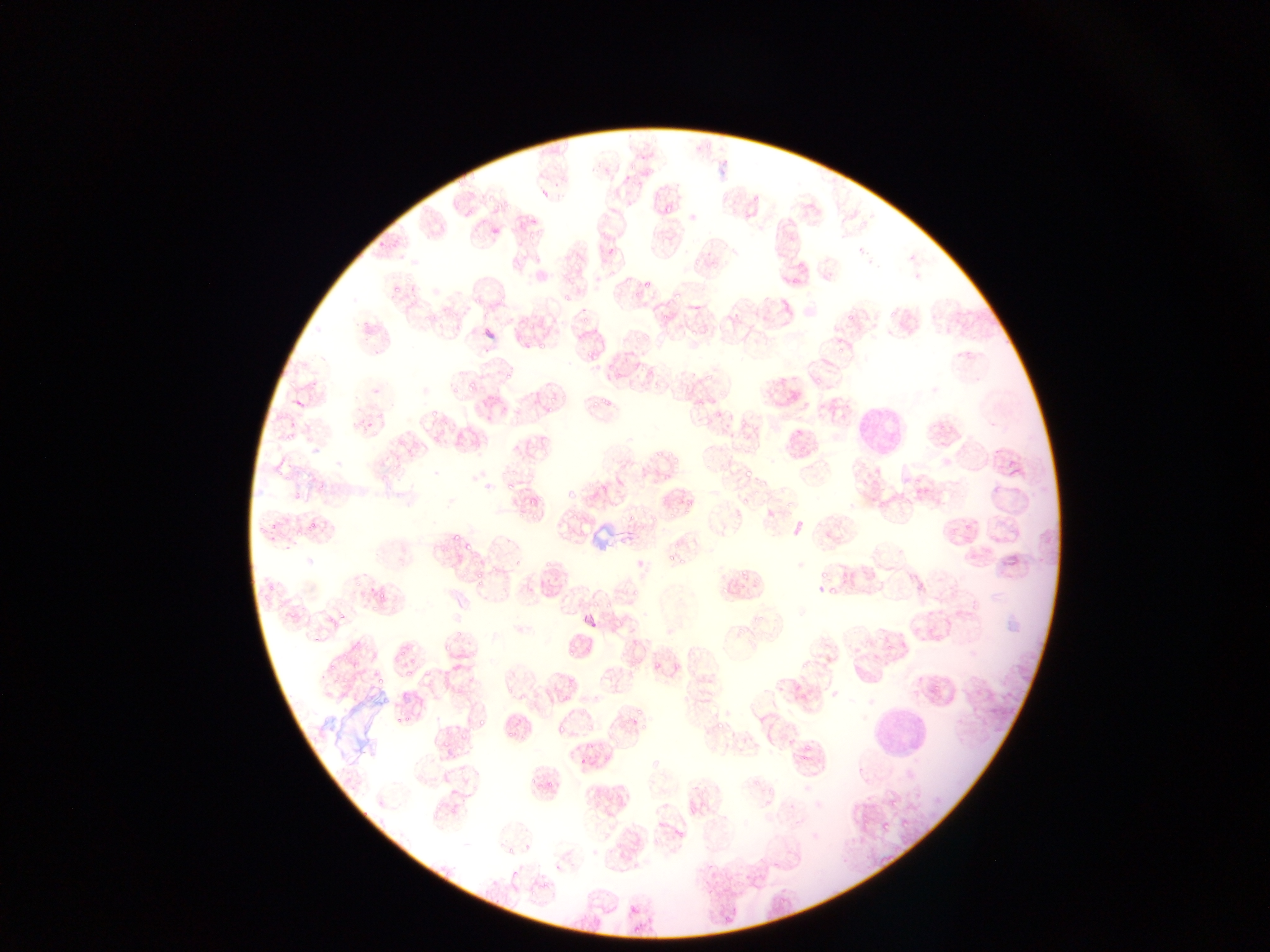 Approximate bounding boxes as left top right bottom in pixels. Plasmodium parasite locations: 539 189 550 200; 661 199 678 213; 531 214 539 224; 604 236 615 268; 643 275 650 290; 562 285 576 304; 577 302 594 324; 524 313 535 322; 534 336 553 350; 578 340 593 364; 502 370 518 384; 462 380 481 396; 547 389 560 406; 603 392 615 412; 427 408 436 422; 363 421 375 434; 284 423 301 438; 784 424 807 449; 656 462 679 487; 741 468 754 481; 314 478 329 492; 502 478 516 503; 563 484 574 504; 307 519 322 536; 270 524 281 539; 450 527 459 539; 459 541 474 556; 668 553 677 561; 352 564 371 594; 815 565 832 578; 372 578 389 601; 329 606 348 627; 564 647 579 658; 651 650 675 672; 324 652 337 672; 402 665 413 674; 566 671 575 688; 364 675 379 693; 392 704 412 730; 634 706 643 716; 505 707 530 743; 476 710 491 728; 716 718 730 735; 553 724 562 734; 453 730 470 747; 439 738 452 759; 579 757 587 766; 546 782 554 793; 898 817 914 832; 878 820 887 833; 553 864 561 873; 629 904 639 915. Leukocyte locations: 356 316 393 353; 855 393 907 453; 865 709 924 751. Image is 1270×952 pixels. Collected in Ghana. Photographed through a microscope with a mobile-phone camera. Single field of view. Thin blood film.